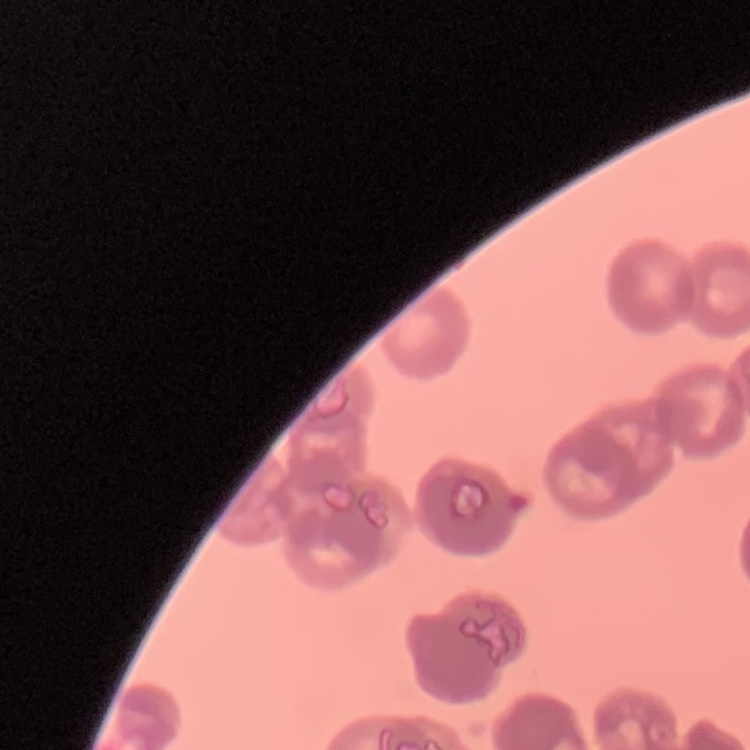

{
  "erythrocyte_morphology": "rouleaux formation",
  "stain": "Field's or Giemsa",
  "image_type": "one tile cut from a larger photomicrograph",
  "preparation": "thin peripheral smear"
}